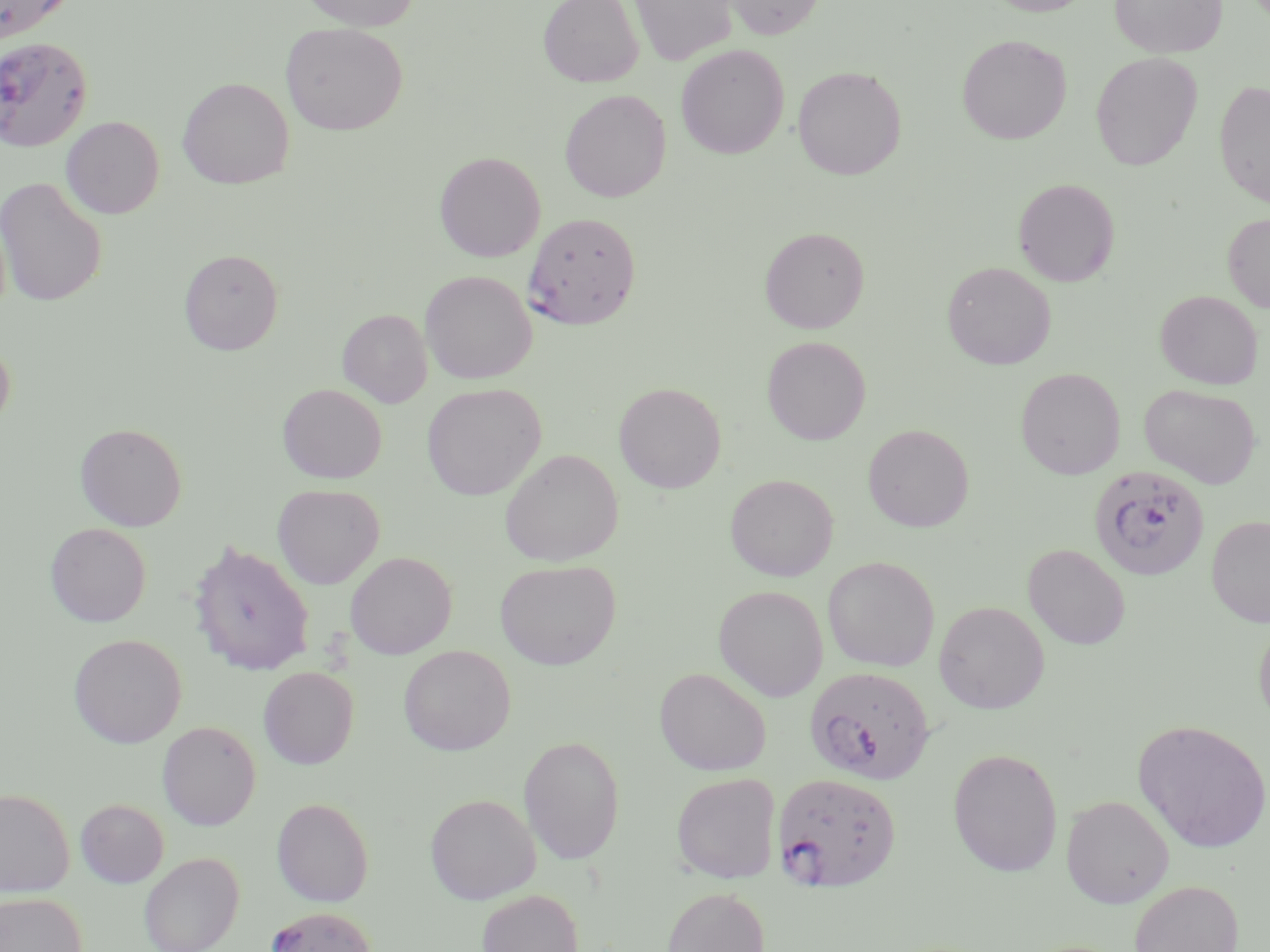

Approximate bounding boxes as (x1,y1)-(x2,y2) corner pairs in pixels. Plasmodium falciparum-infected red blood cell locations: (0,35)-(94,152), (523,212)-(641,329), (1088,465)-(1210,580), (804,665)-(935,786), (771,771)-(902,894), (265,906)-(377,952). Uninfected red blood cell locations: (0,0)-(74,42), (299,0)-(420,31), (538,0)-(643,88), (629,0)-(738,65), (722,0)-(826,40), (983,0)-(1095,16), (1110,0)-(1226,58), (281,22)-(408,136), (957,34)-(1072,144), (675,44)-(789,159), (1090,51)-(1202,170), (675,54)-(905,167), (793,65)-(906,180), (177,77)-(294,189), (1214,80)-(1270,208), (559,89)-(671,202), (61,116)-(165,219), (434,151)-(545,262), (0,176)-(107,307), (1013,178)-(1120,287), (1222,213)-(1270,313), (760,226)-(869,333), (179,249)-(283,354), (942,262)-(1056,369), (420,270)-(537,384), (1155,290)-(1263,389), (338,309)-(432,407), (762,336)-(871,445), (0,337)-(15,433), (1015,367)-(1126,479), (613,381)-(726,493), (277,383)-(387,483), (422,383)-(546,501), (1140,383)-(1261,488), (75,422)-(188,531), (863,424)-(973,532), (500,449)-(623,566), (725,473)-(838,581), (273,484)-(384,589), (1206,516)-(1270,627), (45,522)-(151,627), (188,539)-(315,677), (1023,544)-(1131,650), (345,552)-(457,659), (823,556)-(940,672), (495,559)-(621,669), (714,585)-(828,701), (933,601)-(1050,714), (1253,614)-(1270,733), (68,633)-(187,748), (398,645)-(516,756), (258,666)-(359,769), (654,667)-(772,775), (1134,719)-(1270,853), (157,720)-(261,830), (518,735)-(626,864), (947,748)-(1063,876), (671,773)-(780,883), (0,788)-(75,898), (424,792)-(541,904), (1061,794)-(1174,908), (271,797)-(374,907), (75,799)-(168,888), (139,852)-(245,952), (1128,880)-(1243,952), (661,886)-(770,952), (477,889)-(584,952), (0,892)-(86,952). Slide-level diagnosis: Plasmodium falciparum. May-Grünwald-Giemsa stain. Optical microscopy. Captured at 1000x magnification. Single field of view. Thin blood smear. Image is 1270×952 pixels.